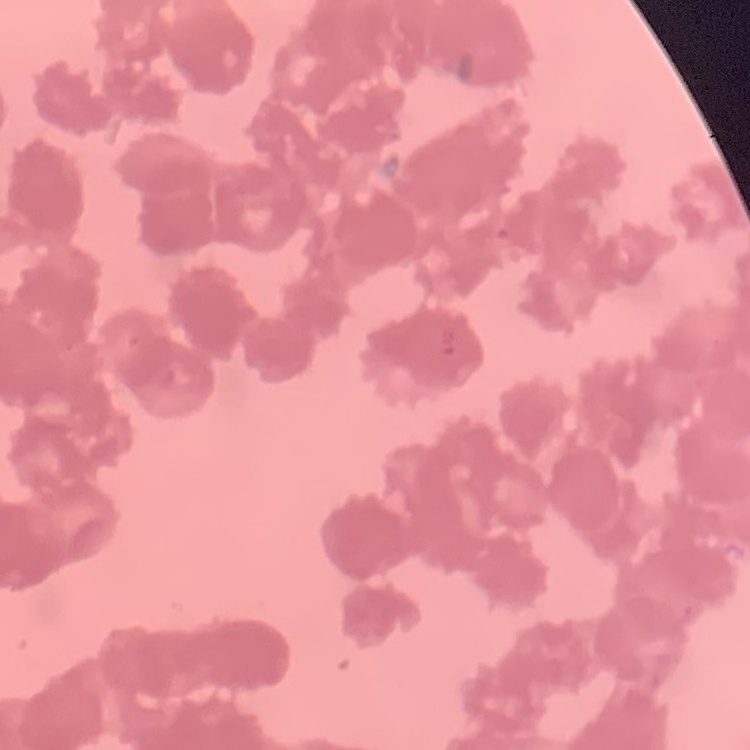

erythrocyte_morphology: rouleaux formation
image_type: square crop of a larger photomicrograph
preparation: thin peripheral smear
stain: Field's or Giemsa